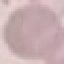

Summary:
  - Malaria status: uninfected
  - Stain: Giemsa
  - Capture: smartphone camera at the microscope eyepiece
  - Preparation: thin blood film
  - Image type: cell patch, automatically extracted from a larger field of view and resized to 64 × 64 pixels